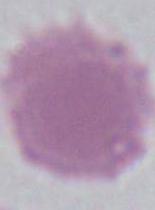
Captured at 1000x magnification. A red blood cell is shown. Photomicrograph.